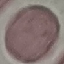

Summary:
  - Malaria status: uninfected
  - Image type: automatically extracted cell patch, resized to 64 × 64 pixels
  - Preparation: thin blood film
  - Capture: smartphone through the microscope eyepiece
  - Stain: Giemsa